Identify the parasite.
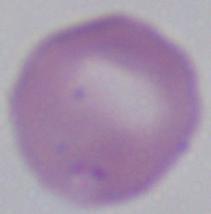
Babesia.

Summary:
  - Modality: photomicrograph
  - Magnification: 1000x